Comment on the morphology of the erythrocytes.
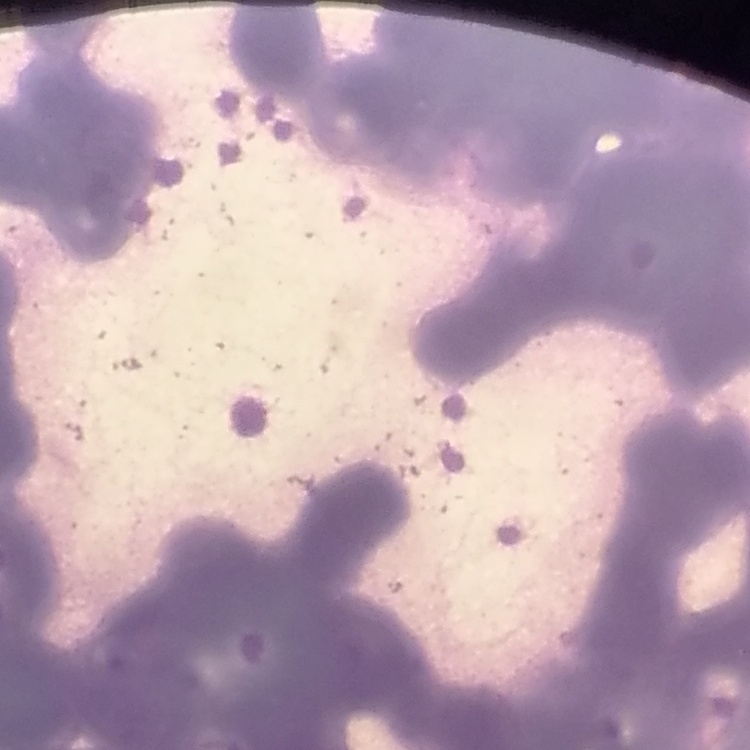
They show rouleaux formation.

Square crop of a larger photomicrograph. Thin peripheral smear. Stained with either Field's or Giemsa.